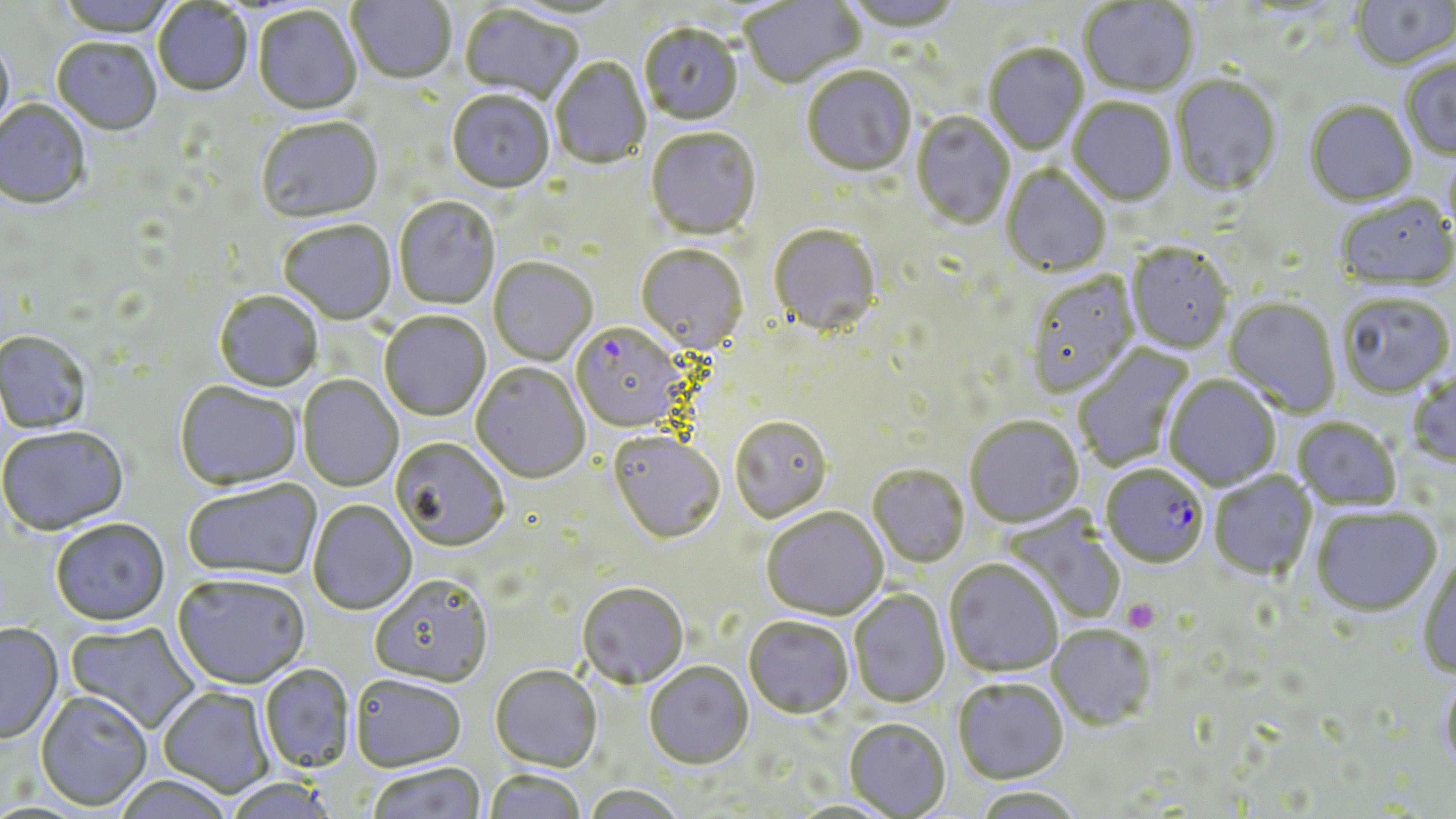

slide-level diagnosis = Plasmodium falciparum
platelet locations = approximate bounding boxes as (x1,y1)-(x2,y2) corner pairs in pixels: (1120,598)-(1162,633)
Plasmodium falciparum-infected red blood cell locations = approximate bounding boxes as (x1,y1)-(x2,y2) corner pairs in pixels: (578,324)-(688,428), (1101,465)-(1209,570)
preparation = thin blood smear
stain = May-Grünwald-Giemsa
image size = 1456×819 pixels
uninfected red blood cell locations = approximate bounding boxes as (x1,y1)-(x2,y2) corner pairs in pixels: (54,0)-(180,39), (347,0)-(455,86), (503,0)-(631,21), (740,0)-(865,90), (842,0)-(966,36), (1350,0)-(1456,72), (1079,1)-(1199,99), (152,2)-(253,99), (459,6)-(584,106), (253,8)-(361,117), (639,26)-(743,127), (0,36)-(15,139), (52,39)-(162,138), (983,45)-(1089,156), (551,57)-(650,170), (1401,57)-(1456,161), (802,67)-(916,179), (1170,75)-(1282,199), (447,92)-(554,195), (1068,99)-(1177,207), (0,100)-(91,212), (1305,102)-(1417,208), (911,112)-(1015,232), (257,120)-(384,225), (645,129)-(762,241), (1001,166)-(1110,276), (1336,197)-(1456,293), (394,198)-(500,310), (278,221)-(396,326), (769,226)-(881,340), (635,245)-(748,357), (1125,246)-(1233,354), (488,259)-(597,367), (1027,274)-(1140,400), (213,292)-(324,393), (1338,296)-(1455,400), (1223,299)-(1340,417), (379,312)-(491,422), (0,332)-(93,436), (1073,343)-(1195,470), (471,363)-(590,484), (1407,372)-(1456,470), (298,376)-(403,492), (1164,377)-(1280,490), (174,382)-(301,492), (730,418)-(832,524), (965,418)-(1083,528), (1293,418)-(1402,511), (0,427)-(130,537), (608,433)-(725,547), (390,440)-(509,552), (868,466)-(969,569), (1209,472)-(1317,581), (183,480)-(321,582), (308,501)-(417,616), (1000,508)-(1127,626), (1311,508)-(1442,617), (761,509)-(887,622), (50,520)-(171,627), (1417,555)-(1456,679), (944,561)-(1063,678), (172,575)-(310,690), (369,576)-(493,689), (577,584)-(688,690), (849,590)-(950,709), (744,618)-(853,721), (64,622)-(200,733), (0,623)-(63,745), (1046,626)-(1157,732), (644,663)-(754,770), (259,665)-(355,774), (490,666)-(602,772), (1439,671)-(1456,779), (350,676)-(466,773), (952,679)-(1068,785), (157,687)-(274,798), (35,692)-(152,812), (845,720)-(950,818), (368,762)-(486,819), (484,770)-(586,819), (112,775)-(237,819), (224,779)-(336,819), (583,785)-(684,819), (971,788)-(1084,818)
modality = light microscopy
magnification = 1000x
field of view = one of a larger specimen